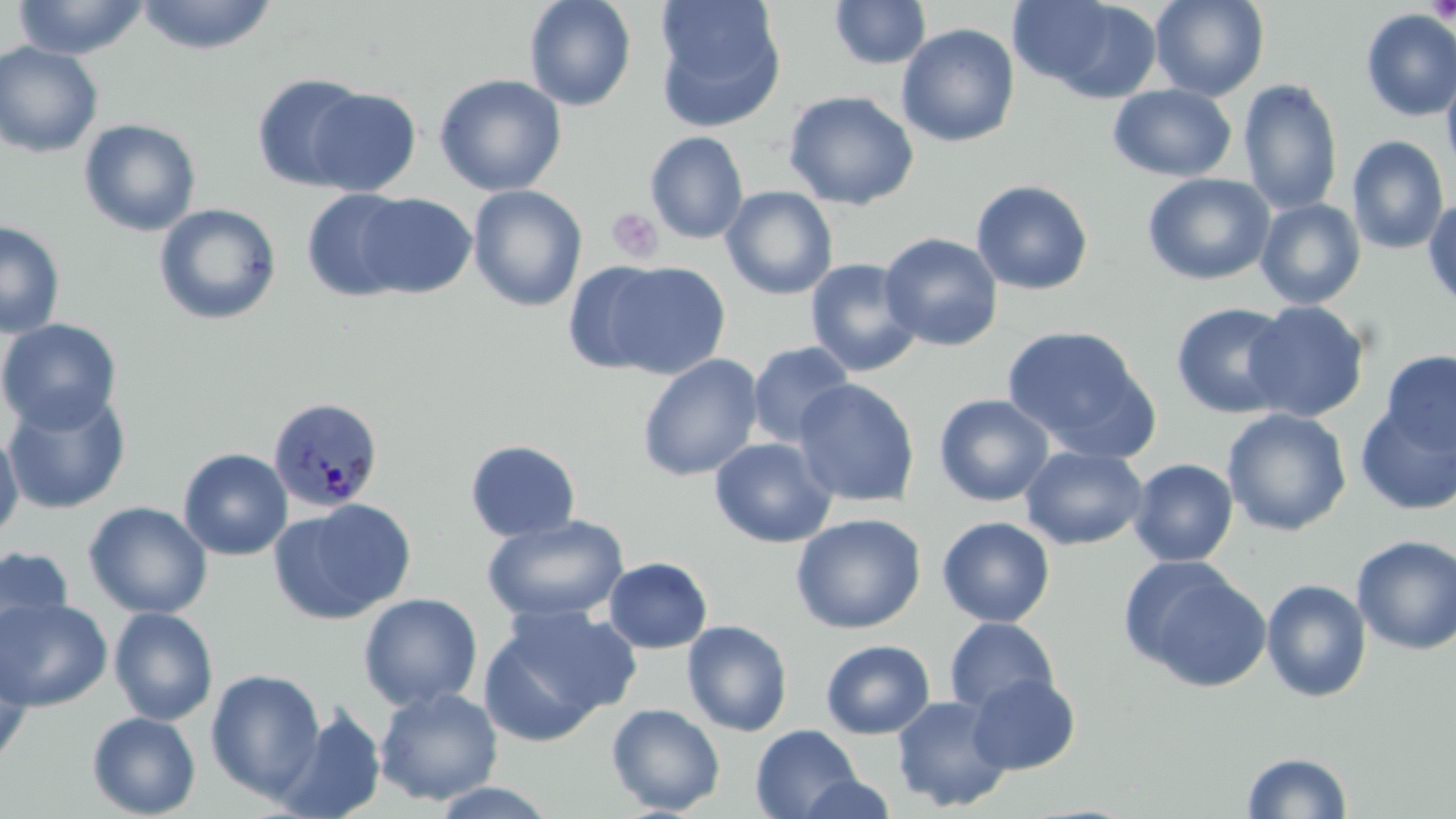

Summary:
  - Coordinate format: approximate bounding boxes as [x1, y1, x2, y2] in pixels
  - Plasmodium malariae-infected red blood cell locations: [267, 396, 384, 512]
  - Platelet locations: [1427, 0, 1456, 23], [606, 207, 663, 264]
  - Uninfected red blood cell locations: [13, 0, 147, 60], [135, 0, 278, 54], [524, 0, 637, 111], [653, 0, 787, 132], [1013, 0, 1163, 102], [1150, 0, 1270, 101], [828, 1, 932, 70], [1360, 9, 1456, 123], [897, 23, 1020, 147], [0, 41, 104, 158], [1441, 64, 1456, 183], [251, 72, 373, 191], [434, 73, 567, 196], [1238, 78, 1343, 215], [1108, 84, 1237, 182], [304, 87, 422, 196], [783, 90, 920, 210], [78, 118, 202, 236], [644, 131, 749, 244], [1346, 135, 1449, 255], [1142, 172, 1276, 285], [970, 179, 1094, 296], [467, 184, 588, 312], [720, 186, 838, 299], [301, 189, 416, 302], [353, 192, 477, 298], [1422, 194, 1456, 313], [1255, 198, 1366, 309], [153, 203, 283, 325], [0, 220, 66, 338], [879, 233, 1004, 351], [805, 258, 924, 378], [598, 261, 731, 378], [563, 262, 674, 375], [1243, 300, 1371, 422], [1171, 302, 1296, 418], [0, 318, 123, 435], [1001, 324, 1157, 458], [746, 340, 856, 447], [1379, 350, 1456, 456], [637, 353, 764, 481], [793, 378, 920, 508], [2, 391, 132, 515], [934, 394, 1054, 506], [1356, 402, 1456, 516], [1222, 408, 1352, 537], [0, 427, 24, 544], [709, 436, 837, 548], [464, 439, 581, 543], [1020, 445, 1148, 550], [178, 448, 293, 560], [1129, 458, 1238, 567], [268, 499, 417, 626], [83, 501, 212, 619], [790, 513, 926, 634], [482, 515, 630, 624], [937, 516, 1056, 626], [1351, 535, 1456, 656], [0, 545, 74, 658], [1120, 555, 1271, 692], [604, 557, 713, 654], [1261, 578, 1372, 703], [358, 593, 483, 712], [1, 596, 112, 712], [479, 605, 636, 744], [108, 607, 219, 725], [944, 617, 1059, 716], [682, 620, 793, 737], [0, 636, 34, 770], [820, 639, 935, 739], [206, 668, 326, 801], [966, 672, 1080, 774], [374, 686, 503, 806], [891, 694, 1013, 812], [606, 702, 726, 815], [274, 704, 387, 819], [87, 711, 201, 818], [750, 724, 863, 819], [1241, 751, 1353, 818], [795, 773, 899, 817], [428, 781, 560, 818]
  - Slide-level diagnosis: Plasmodium malariae
  - Field of view: one of a larger specimen
  - Image size: 1456×819 pixels
  - Magnification: 1000x
  - Stain: May-Grünwald-Giemsa
  - Preparation: thin blood film
  - Modality: optical microscopy